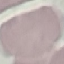

Malaria status: uninfected. Giemsa stain. Thin blood smear. Automatically extracted cell patch, resized to 64 × 64 pixels. Photographed with a smartphone camera at the microscope eyepiece.